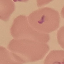

Summary:
  - Malaria status: uninfected
  - Stain: Giemsa
  - Image type: cell patch, automatically extracted from a larger field of view and resized to 64 × 64 pixels
  - Preparation: thin smear
  - Capture: smartphone camera at the microscope eyepiece